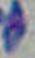
identification = Toxoplasma gondii
magnification = 1000x
modality = micrograph